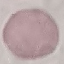

Summary:
  - Result: no malaria parasites detected
  - Preparation: thin smear
  - Capture: smartphone camera at the microscope eyepiece
  - Stain: Giemsa
  - Image type: cell patch, automatically extracted from a larger field of view and resized to 64 × 64 pixels